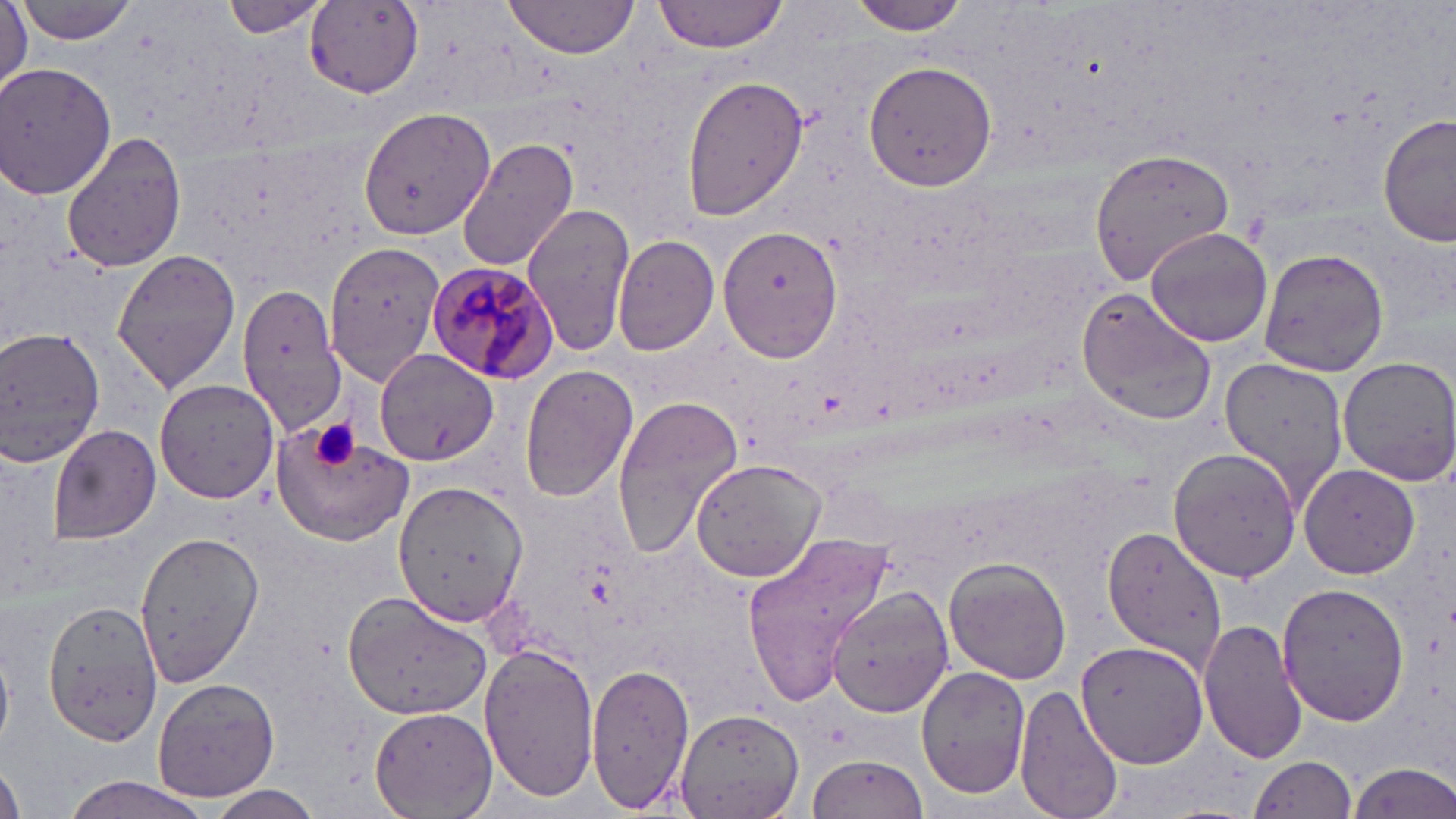
Summary:
  - Coordinate format: approximate bounding boxes as [x1, y1, x2, y2] in pixels
  - Uninfected red blood cell locations: [505, 0, 641, 58], [654, 0, 790, 51], [844, 0, 974, 35], [15, 1, 142, 45], [0, 2, 29, 95], [218, 2, 330, 38], [304, 4, 424, 98], [864, 59, 998, 192], [1, 62, 118, 200], [679, 74, 807, 221], [359, 106, 495, 241], [1378, 113, 1454, 249], [62, 130, 186, 273], [457, 136, 580, 272], [1089, 145, 1242, 285], [522, 202, 634, 358], [714, 223, 845, 365], [1144, 227, 1274, 348], [613, 235, 721, 355], [326, 241, 448, 384], [111, 245, 241, 395], [1258, 248, 1390, 376], [236, 285, 350, 432], [1077, 290, 1217, 426], [0, 326, 106, 471], [374, 347, 500, 465], [1218, 355, 1350, 511], [1335, 356, 1456, 485], [519, 363, 639, 504], [153, 378, 280, 503], [610, 392, 743, 561], [271, 419, 417, 546], [47, 423, 162, 544], [1167, 449, 1301, 580], [690, 458, 826, 583], [1301, 465, 1421, 579], [393, 479, 526, 627], [1101, 525, 1229, 668], [133, 527, 263, 689], [740, 531, 894, 708], [945, 557, 1072, 684], [1275, 583, 1409, 725], [828, 586, 953, 718], [344, 589, 491, 722], [40, 601, 162, 745], [1199, 619, 1307, 764], [1073, 638, 1208, 769], [0, 640, 15, 751], [479, 644, 598, 802], [586, 663, 696, 813], [916, 664, 1029, 799], [152, 676, 280, 804], [1014, 683, 1125, 819], [368, 705, 497, 819], [673, 710, 805, 818], [1249, 754, 1358, 818], [807, 755, 928, 819], [0, 761, 28, 819], [1345, 761, 1456, 819], [57, 775, 217, 819], [202, 786, 328, 818]
  - Platelet locations: [312, 421, 363, 469]
  - Plasmodium malariae-infected red blood cell locations: [426, 261, 556, 383]
  - Slide-level diagnosis: Plasmodium malariae
  - Magnification: 1000x
  - Image size: 1456×819 pixels
  - Field of view: one of a larger specimen
  - Preparation: thin blood smear
  - Stain: May-Grünwald-Giemsa
  - Modality: light microscopy